Assess this cell for malaria.
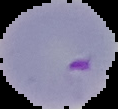
Parasitized.

From a thin blood smear. Segmented cell region on a black background. Image is 118×109 pixels.